Assess this cell for malaria.
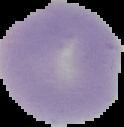
It is uninfected.

Summary:
  - Image size: 124×127 pixels
  - Preparation: thin blood smear
  - Image type: segmented cell region with the area outside set to black